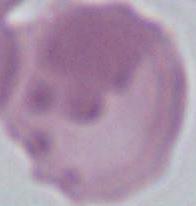
{
  "modality": "micrograph",
  "identification": "red blood cell",
  "magnification": "1000x"
}